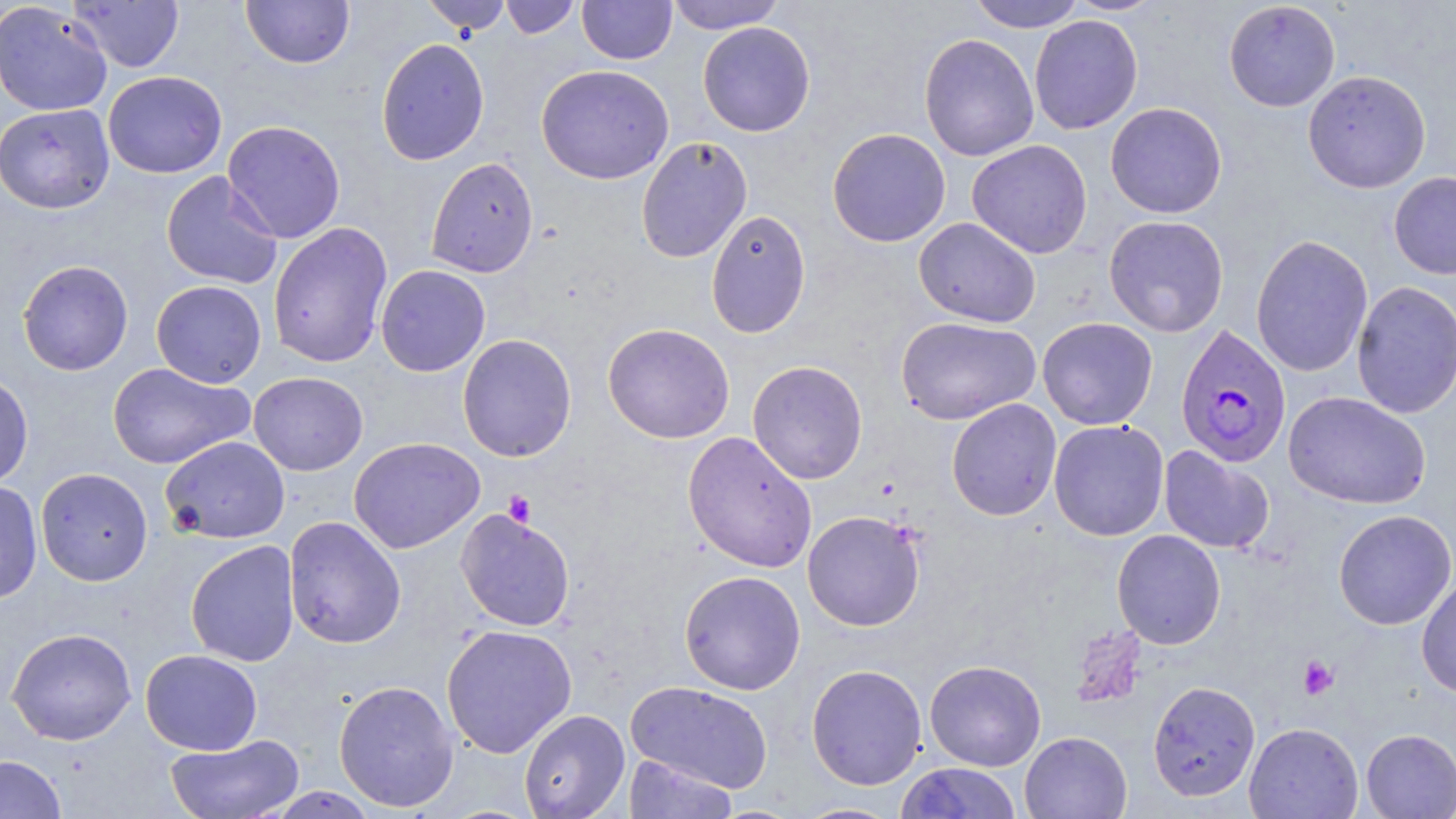

slide_level_diagnosis: Plasmodium falciparum
magnification: 1000x
stain: May-Grünwald-Giemsa
modality: light microscopy
image_size: 1456×819 pixels
preparation: thin blood smear
uninfected_red_blood_cell_locations: 'approximate bounding boxes as (x1,y1)-(x2,y2) corner pairs in pixels: (69,0)-(185,73), (241,0)-(355,69), (420,0)-(512,35), (500,0)-(581,39), (577,0)-(677,65), (665,0)-(786,34), (967,0)-(1086,31), (0,1)-(113,117), (1223,1)-(1341,112), (1029,15)-(1143,134), (698,21)-(815,137), (919,33)-(1039,162), (376,37)-(490,166), (536,63)-(674,185), (103,70)-(227,178), (1302,70)-(1431,194), (1105,102)-(1227,218), (0,103)-(115,214), (222,120)-(345,243), (827,127)-(951,247), (636,136)-(753,263), (966,139)-(1093,259), (425,157)-(539,278), (161,170)-(283,289), (1388,171)-(1456,279), (705,208)-(811,338), (1103,215)-(1229,337), (913,217)-(1041,328), (268,221)-(393,368), (1251,234)-(1373,377), (18,259)-(133,376), (375,264)-(491,376), (151,280)-(267,388), (1351,281)-(1456,419), (895,316)-(1040,424), (1037,317)-(1158,430), (602,323)-(735,444), (457,333)-(577,462), (747,360)-(868,484), (107,363)-(253,469), (248,372)-(368,476), (0,373)-(33,489), (1283,391)-(1431,510), (946,398)-(1062,521), (1048,420)-(1169,541), (681,431)-(817,573), (160,435)-(290,543), (348,437)-(485,554), (1159,445)-(1274,554), (35,467)-(153,586), (0,480)-(42,603), (456,507)-(575,632), (802,510)-(926,631), (1333,510)-(1456,630), (283,516)-(406,649), (1111,529)-(1226,649), (185,540)-(299,667), (679,570)-(805,694), (1416,577)-(1456,697), (441,623)-(577,758), (6,627)-(137,745), (140,649)-(262,754), (924,659)-(1046,771), (806,663)-(927,790), (333,680)-(459,811), (625,680)-(774,793), (1148,680)-(1261,802), (518,709)-(630,819), (1244,722)-(1363,819), (1361,729)-(1456,818), (1019,731)-(1132,818), (165,734)-(303,818), (0,754)-(67,818), (622,754)-(739,818), (896,762)-(1024,818), (262,787)-(380,818), (793,801)-(903,819)'
field_of_view: single
plasmodium_falciparum_infected_red_blood_cell_locations: 'approximate bounding boxes as (x1,y1)-(x2,y2) corner pairs in pixels: (1175,324)-(1291,468)'
platelet_locations: 'approximate bounding boxes as (x1,y1)-(x2,y2) corner pairs in pixels: (502,490)-(537,527), (1298,655)-(1339,700)'